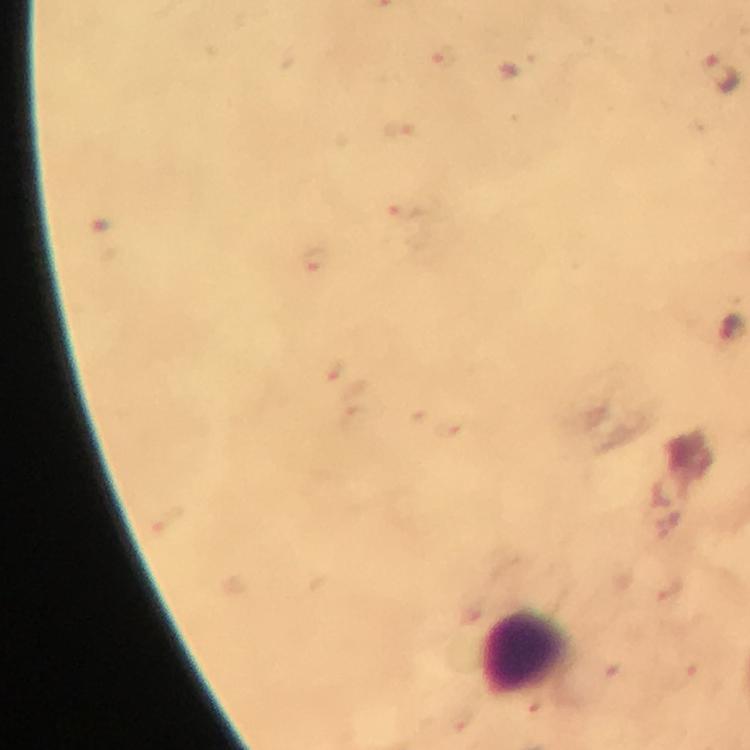 Approximate centers as {x, y} in pixels. Plasmodium parasite locations: {723, 73}. Leukocyte locations: {527, 653}. 100x magnification. Image is 750×750 pixels. Giemsa stain. Photographed through the microscope with a smartphone camera. Immersion oil was used. A crop from one field of view. Thick smear. From a malaria diagnostic workup.